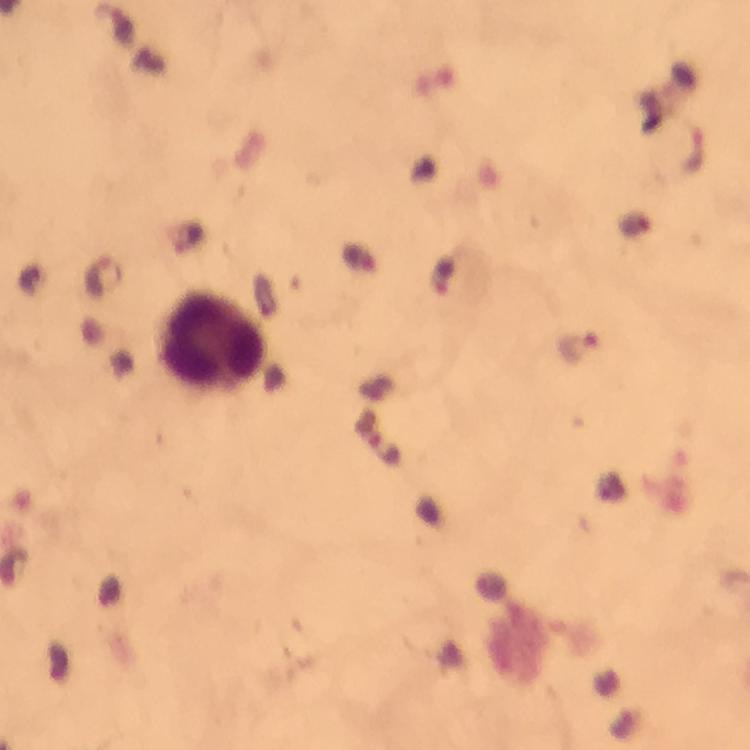

Approximate centers as (x, y) in pixels. Plasmodium parasite locations: (106, 276), (579, 348). Leukocyte locations: (212, 339). At 100x magnification. Photographed with a smartphone mounted on the microscope. Immersion oil was used. Thick blood smear. A crop from one field of view. Giemsa stain. Image is 750×750 pixels. From a diagnostic examination for malaria.